Name the cell type shown.
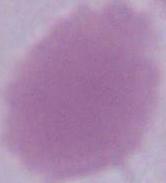
An erythrocyte.

modality: micrograph
magnification: 1000x